Name the blood parasite species.
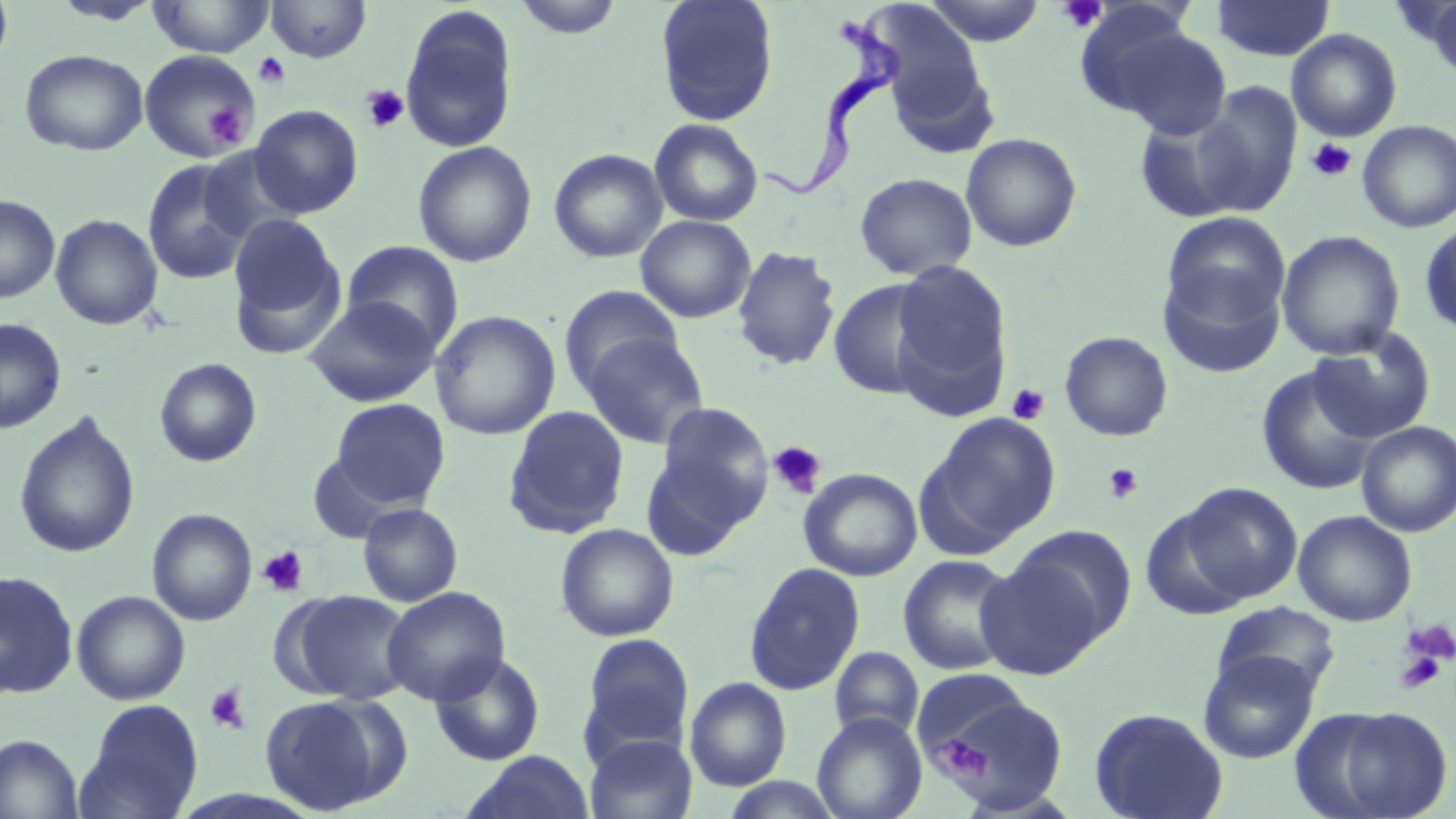

Trypanosoma brucei.

preparation = thin blood smear
uninfected red blood cell locations = approximate bounding boxes as named x1/y1/x2/y2 corners in pixels: (x1=0, y1=0, x2=14, y2=78), (x1=49, y1=0, x2=163, y2=25), (x1=146, y1=0, x2=274, y2=58), (x1=513, y1=0, x2=625, y2=39), (x1=655, y1=0, x2=780, y2=127), (x1=922, y1=0, x2=1046, y2=46), (x1=265, y1=1, x2=372, y2=63), (x1=1211, y1=1, x2=1335, y2=62), (x1=1416, y1=1, x2=1456, y2=81), (x1=863, y1=2, x2=989, y2=121), (x1=399, y1=7, x2=519, y2=154), (x1=1095, y1=20, x2=1231, y2=139), (x1=1286, y1=28, x2=1403, y2=141), (x1=884, y1=48, x2=999, y2=160), (x1=19, y1=49, x2=148, y2=156), (x1=140, y1=49, x2=259, y2=160), (x1=1190, y1=82, x2=1302, y2=218), (x1=250, y1=104, x2=364, y2=218), (x1=1132, y1=107, x2=1253, y2=223), (x1=649, y1=118, x2=764, y2=227), (x1=1357, y1=120, x2=1456, y2=233), (x1=960, y1=132, x2=1083, y2=252), (x1=412, y1=140, x2=537, y2=267), (x1=198, y1=145, x2=307, y2=244), (x1=548, y1=147, x2=668, y2=263), (x1=142, y1=159, x2=253, y2=285), (x1=854, y1=172, x2=977, y2=281), (x1=0, y1=194, x2=60, y2=303), (x1=1161, y1=212, x2=1291, y2=333), (x1=50, y1=213, x2=163, y2=330), (x1=227, y1=215, x2=346, y2=354), (x1=635, y1=215, x2=757, y2=323), (x1=1419, y1=219, x2=1456, y2=337), (x1=1276, y1=230, x2=1406, y2=361), (x1=341, y1=240, x2=465, y2=352), (x1=731, y1=245, x2=842, y2=371), (x1=890, y1=260, x2=1013, y2=412), (x1=1157, y1=264, x2=1286, y2=379), (x1=828, y1=278, x2=942, y2=400), (x1=559, y1=284, x2=684, y2=396), (x1=304, y1=296, x2=440, y2=407), (x1=430, y1=309, x2=561, y2=441), (x1=0, y1=318, x2=66, y2=434), (x1=1309, y1=329, x2=1437, y2=442), (x1=582, y1=331, x2=709, y2=449), (x1=1059, y1=331, x2=1174, y2=442), (x1=154, y1=357, x2=262, y2=467), (x1=1256, y1=362, x2=1382, y2=496), (x1=331, y1=398, x2=450, y2=508), (x1=652, y1=401, x2=773, y2=536), (x1=503, y1=405, x2=630, y2=538), (x1=13, y1=411, x2=141, y2=559), (x1=923, y1=411, x2=1062, y2=549), (x1=1356, y1=421, x2=1456, y2=537), (x1=641, y1=448, x2=755, y2=563), (x1=307, y1=452, x2=407, y2=543), (x1=798, y1=467, x2=923, y2=582), (x1=1176, y1=481, x2=1302, y2=605), (x1=358, y1=503, x2=463, y2=607), (x1=147, y1=508, x2=258, y2=626), (x1=1292, y1=510, x2=1417, y2=627), (x1=555, y1=523, x2=679, y2=642), (x1=1004, y1=524, x2=1137, y2=647), (x1=974, y1=551, x2=1110, y2=679), (x1=898, y1=554, x2=1021, y2=675), (x1=743, y1=562, x2=866, y2=696), (x1=0, y1=570, x2=78, y2=698), (x1=381, y1=586, x2=511, y2=705), (x1=71, y1=590, x2=190, y2=705), (x1=286, y1=590, x2=413, y2=704), (x1=1211, y1=601, x2=1342, y2=699), (x1=580, y1=633, x2=695, y2=757), (x1=829, y1=646, x2=924, y2=740), (x1=1198, y1=649, x2=1320, y2=764), (x1=429, y1=652, x2=545, y2=766), (x1=925, y1=675, x2=1068, y2=810), (x1=684, y1=677, x2=792, y2=791), (x1=259, y1=694, x2=397, y2=815), (x1=77, y1=699, x2=204, y2=819), (x1=1296, y1=704, x2=1455, y2=819), (x1=1088, y1=706, x2=1229, y2=819), (x1=812, y1=712, x2=927, y2=819), (x1=584, y1=733, x2=697, y2=819), (x1=0, y1=734, x2=84, y2=819), (x1=463, y1=750, x2=595, y2=818), (x1=719, y1=775, x2=844, y2=818)
field of view = one of a larger specimen
magnification = 1000x
image size = 1456×819 pixels
Trypanosoma brucei locations = approximate bounding boxes as named x1/y1/x2/y2 corners in pixels: (x1=762, y1=15, x2=907, y2=210)
stain = May-Grünwald-Giemsa
modality = optical microscopy
platelet locations = approximate bounding boxes as named x1/y1/x2/y2 corners in pixels: (x1=1056, y1=0, x2=1107, y2=33), (x1=254, y1=53, x2=290, y2=87), (x1=361, y1=84, x2=409, y2=133), (x1=205, y1=104, x2=248, y2=147), (x1=1307, y1=138, x2=1357, y2=183), (x1=1007, y1=383, x2=1050, y2=425), (x1=768, y1=441, x2=827, y2=499), (x1=1103, y1=462, x2=1144, y2=504), (x1=257, y1=546, x2=309, y2=597), (x1=1402, y1=619, x2=1456, y2=668), (x1=1395, y1=646, x2=1447, y2=695), (x1=204, y1=683, x2=250, y2=734), (x1=940, y1=736, x2=990, y2=783)